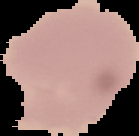

The area outside the segmented cell region is set to black. From a thin blood smear. Image is 139×136 pixels. Result: no malaria parasites seen.